Name the parasite shown.
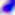

This is Toxoplasma gondii.

Summary:
  - Magnification: 400x
  - Modality: photomicrograph